Name the parasite shown.
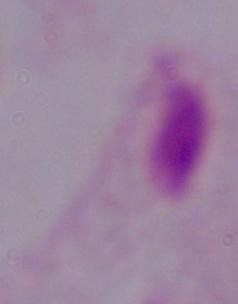
A trichomonad.

modality = photomicrograph
magnification = 1000x